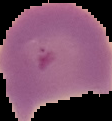
image size = 112×121 pixels
image type = segmented cell region on a black background
preparation = thin blood film
result = malaria parasites detected